Report the malaria status of this cell.
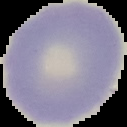

It is uninfected.

image size = 127×127 pixels
image type = segmented cell region on a black background
preparation = thin blood film